Point out each leukocyte.
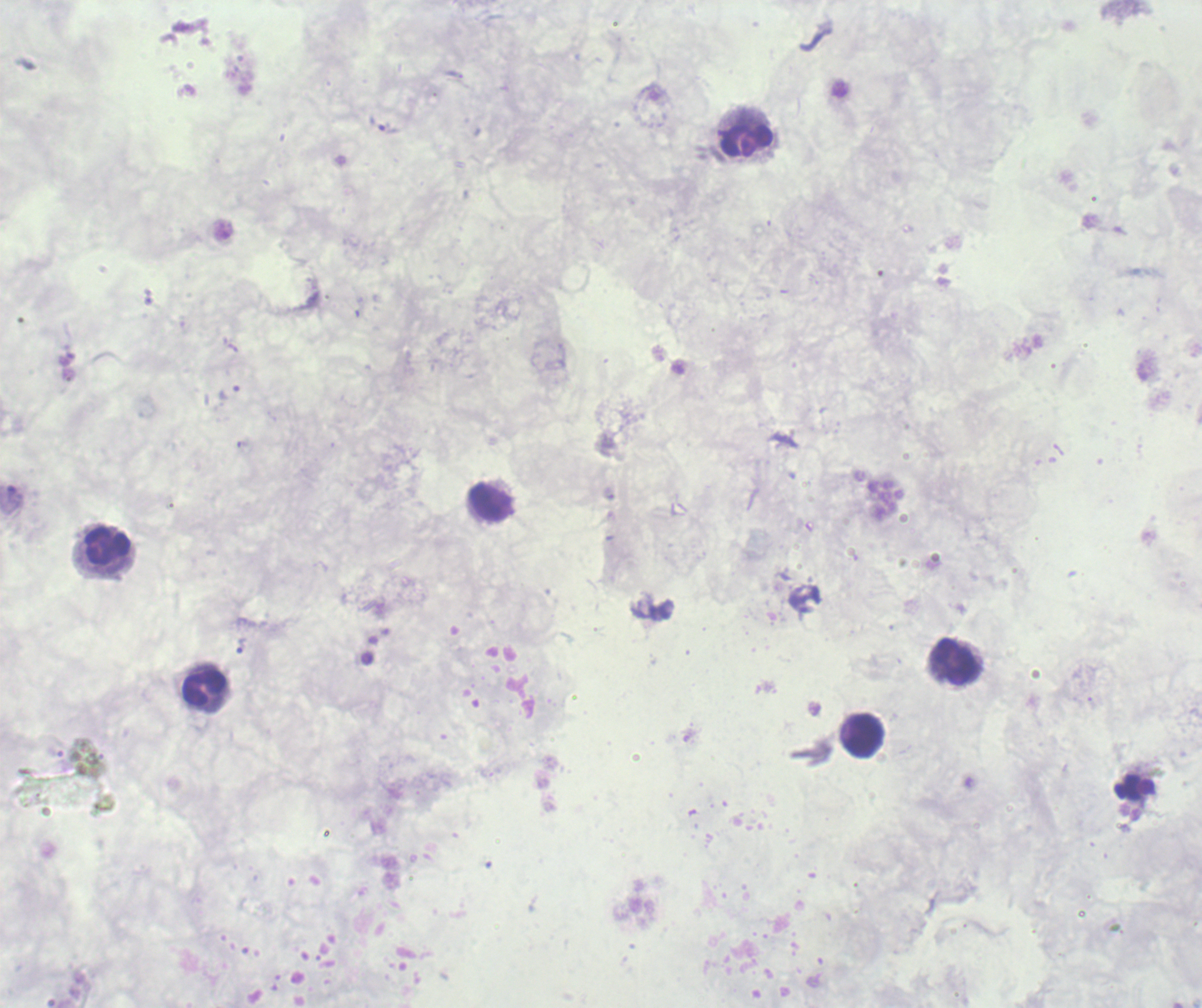
Approximate centers as {x, y} in pixels.
Leukocytes: {747, 142}, {492, 502}, {107, 546}, {955, 661}, {205, 689}, {865, 736}.

coordinate format = approximate centers as {x, y} in pixels
trophozoite locations = {241, 646}
result = malaria parasites detected
field of view = single
stain = Romanowsky
image size = 1202×1008 pixels
preparation = thick blood smear
background quality = unsatisfactory
magnification = 100x
context = previously used in an actual diagnosis